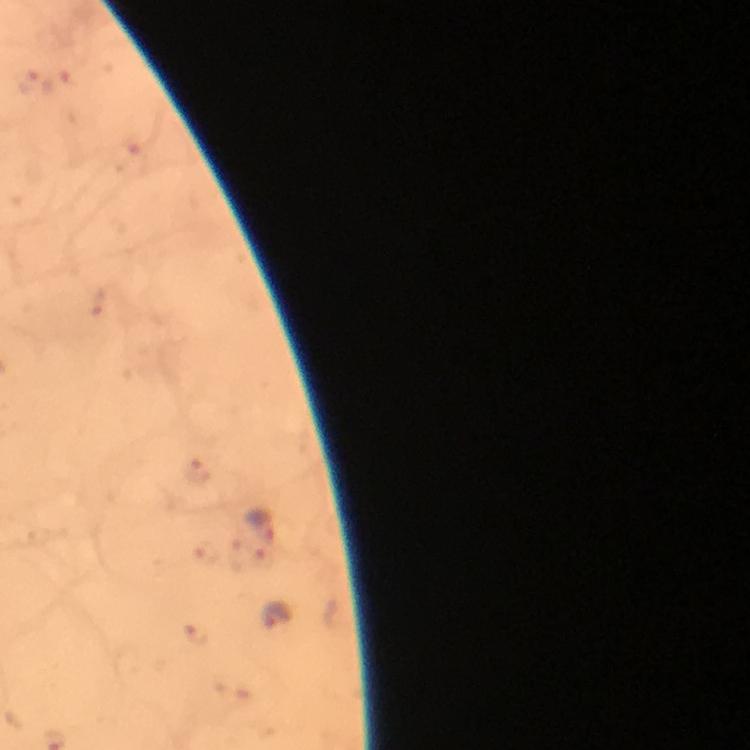

malaria parasite locations = approximate centers as [x, y] in pixels: [263, 524], [277, 615]
preparation = thick blood film
immersion oil = applied
image size = 750×750 pixels
capture = smartphone camera through the microscope
magnification = 100x
context = from a malaria diagnostic workup
stain = Giemsa
cropped from = one field of view